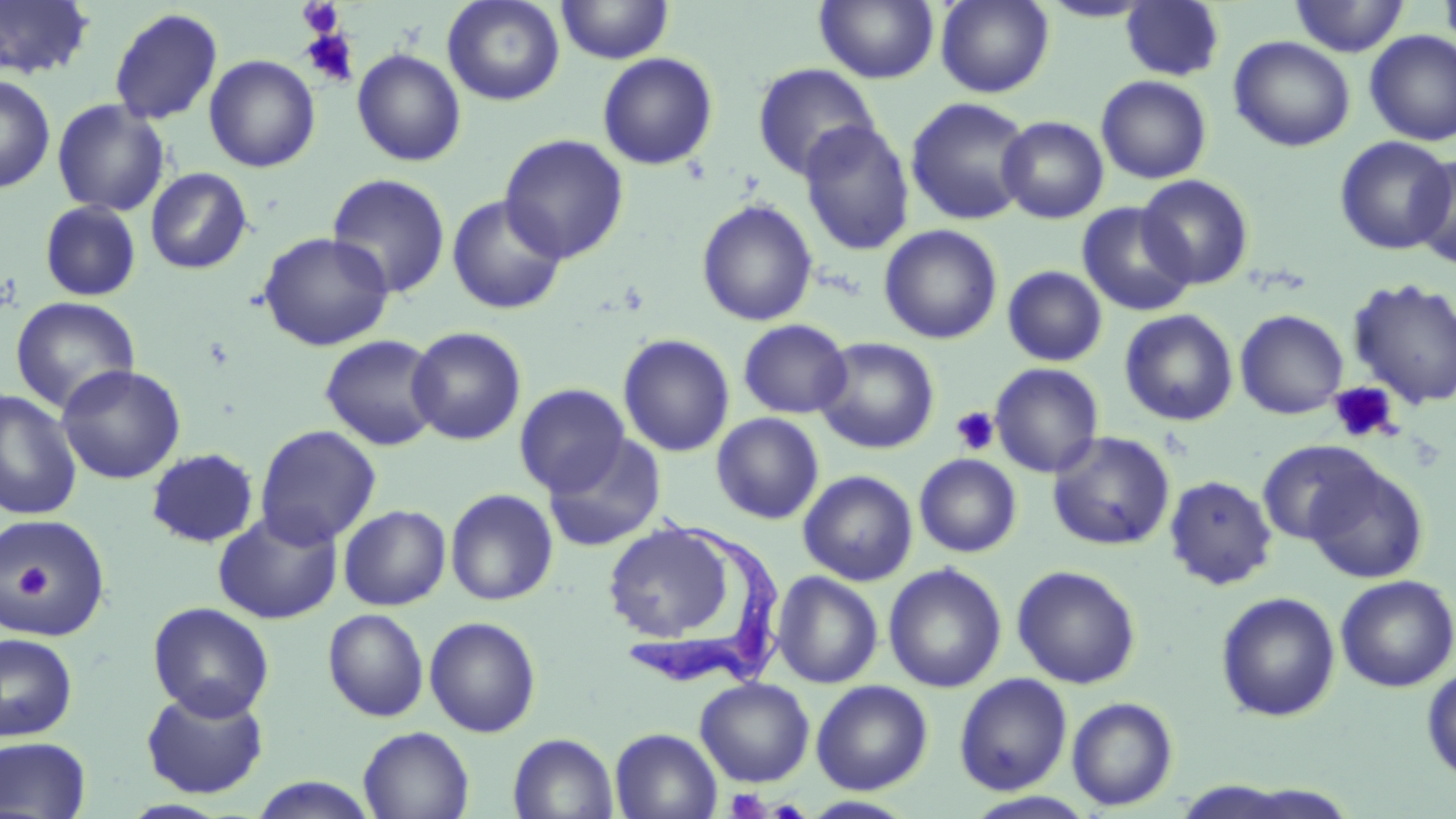

Summary:
  - Coordinate format: approximate bounding boxes as (x1,y1)-(x2,y2) corner pairs in pixels
  - Trypanosoma brucei locations: (626,509)-(789,694)
  - Platelet locations: (297,1)-(344,37), (299,27)-(360,88), (1329,382)-(1400,444), (950,406)-(999,455), (8,561)-(52,602), (725,788)-(770,818)
  - Uninfected red blood cell locations: (442,0)-(565,106), (557,0)-(673,64), (814,0)-(939,84), (935,0)-(1054,97), (1038,0)-(1157,23), (1289,0)-(1409,57), (1438,0)-(1456,57), (0,1)-(96,81), (1120,1)-(1225,81), (109,7)-(223,125), (1364,31)-(1456,146), (1228,35)-(1355,152), (351,48)-(467,167), (597,52)-(719,170), (203,55)-(321,173), (751,62)-(881,181), (0,74)-(56,194), (1095,75)-(1212,184), (905,97)-(1033,226), (51,99)-(170,216), (997,115)-(1109,223), (799,117)-(1034,240), (798,121)-(915,256), (499,133)-(629,264), (1334,136)-(1453,256), (1409,153)-(1456,269), (145,167)-(253,275), (326,173)-(451,298), (1136,174)-(1255,290), (446,194)-(567,316), (697,199)-(817,327), (39,200)-(142,302), (1077,202)-(1196,317), (879,224)-(1003,344), (258,231)-(394,352), (1002,265)-(1108,366), (1348,278)-(1456,410), (11,296)-(140,416), (1119,309)-(1238,426), (1235,309)-(1348,419), (738,318)-(851,419), (406,326)-(527,445), (320,333)-(443,451), (617,333)-(735,457), (814,337)-(940,454), (990,362)-(1104,478), (56,364)-(186,484), (514,383)-(630,496), (0,389)-(82,521), (0,391)-(96,638), (711,412)-(824,525), (255,424)-(381,547), (1047,431)-(1175,551), (542,434)-(668,552), (1256,440)-(1381,547), (145,448)-(260,549), (914,454)-(1022,557), (1302,459)-(1429,584), (798,470)-(918,586), (1164,474)-(1278,591), (445,488)-(559,605), (338,504)-(451,611), (212,510)-(343,625), (1,513)-(112,643), (601,519)-(743,653), (883,563)-(1007,693), (1011,564)-(1142,689), (771,571)-(883,688), (1335,574)-(1456,692), (1215,591)-(1341,722), (148,602)-(274,721), (322,608)-(430,722), (424,615)-(542,738), (0,633)-(78,742), (1422,664)-(1455,784), (954,673)-(1073,795), (694,677)-(814,787), (812,679)-(933,794), (141,686)-(269,799), (1066,696)-(1179,811), (358,726)-(474,819), (610,728)-(722,819), (508,733)-(619,819), (0,736)-(91,819), (247,776)-(380,818), (962,791)-(1098,818), (800,796)-(919,818)
  - Slide-level diagnosis: Trypanosoma brucei
  - Stain: May-Grünwald-Giemsa
  - Magnification: 1000x
  - Modality: optical microscopy
  - Field of view: single
  - Image size: 1456×819 pixels
  - Preparation: thin blood film